State which parasite is depicted.
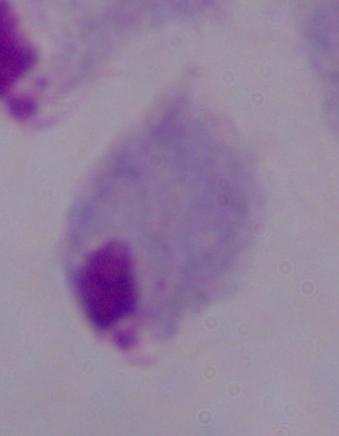

This is a trichomonad.

Summary:
  - Modality: photomicrograph
  - Magnification: 1000x